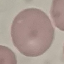
Result: negative for malaria parasites. Giemsa-stained preparation. Automatically extracted cell patch, resized to 64 × 64 pixels. Photographed with a smartphone camera at the microscope eyepiece. Thin smear of blood.